Report the malaria status of this cell.
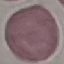

Uninfected.

Photographed with a smartphone camera at the microscope eyepiece. Cell patch, automatically extracted from a larger field of view and resized to 64 × 64 pixels. Giemsa-stained preparation. Thin blood smear.